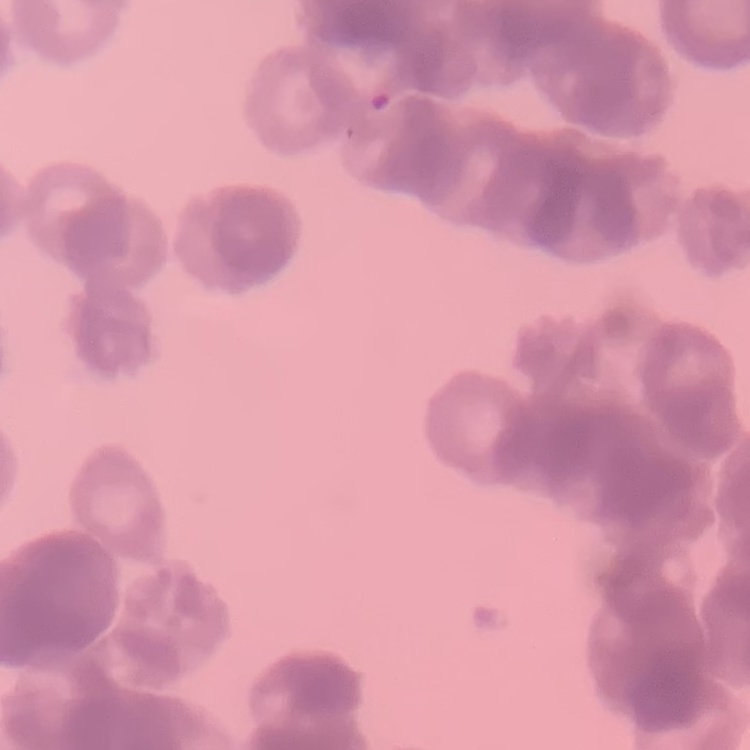
erythrocyte morphology = rouleaux formation
image type = one tile cut from a larger photomicrograph
preparation = thin blood film
stain = Field's or Giemsa